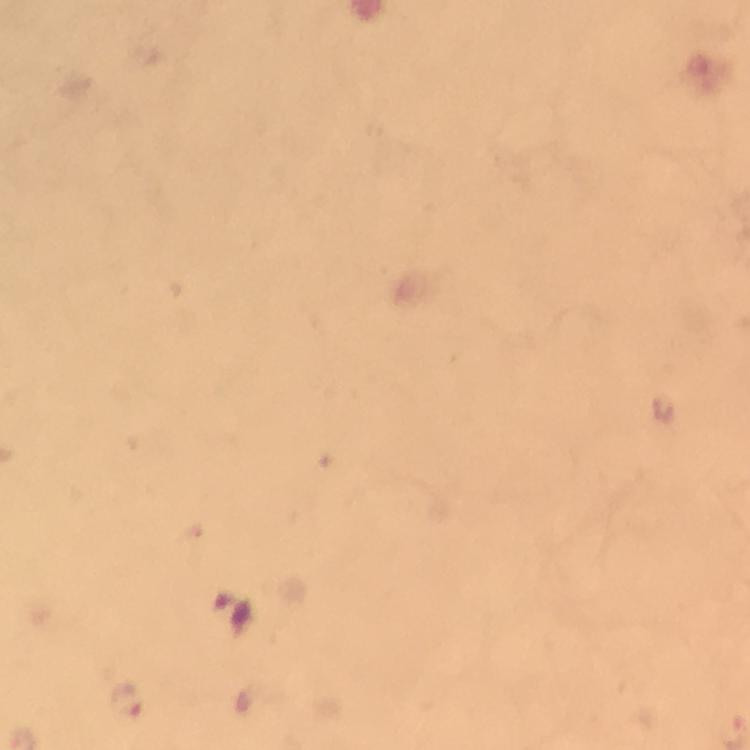

{
  "stain": "Giemsa",
  "preparation": "thick blood film",
  "magnification": "100x",
  "cropped_from": "one field of view",
  "plasmodium_parasite_locations": "approximate object centers, in pixels from the top-left corner: (x=127, y=701)",
  "capture": "smartphone mounted on the microscope",
  "image_size": "750×750 pixels",
  "immersion_oil": "used",
  "context": "from a malaria diagnostic workup"
}